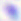

Photomicrograph. Toxoplasma gondii is seen. 400x magnification.